Give the position of every malaria parasite and every leukocyte.
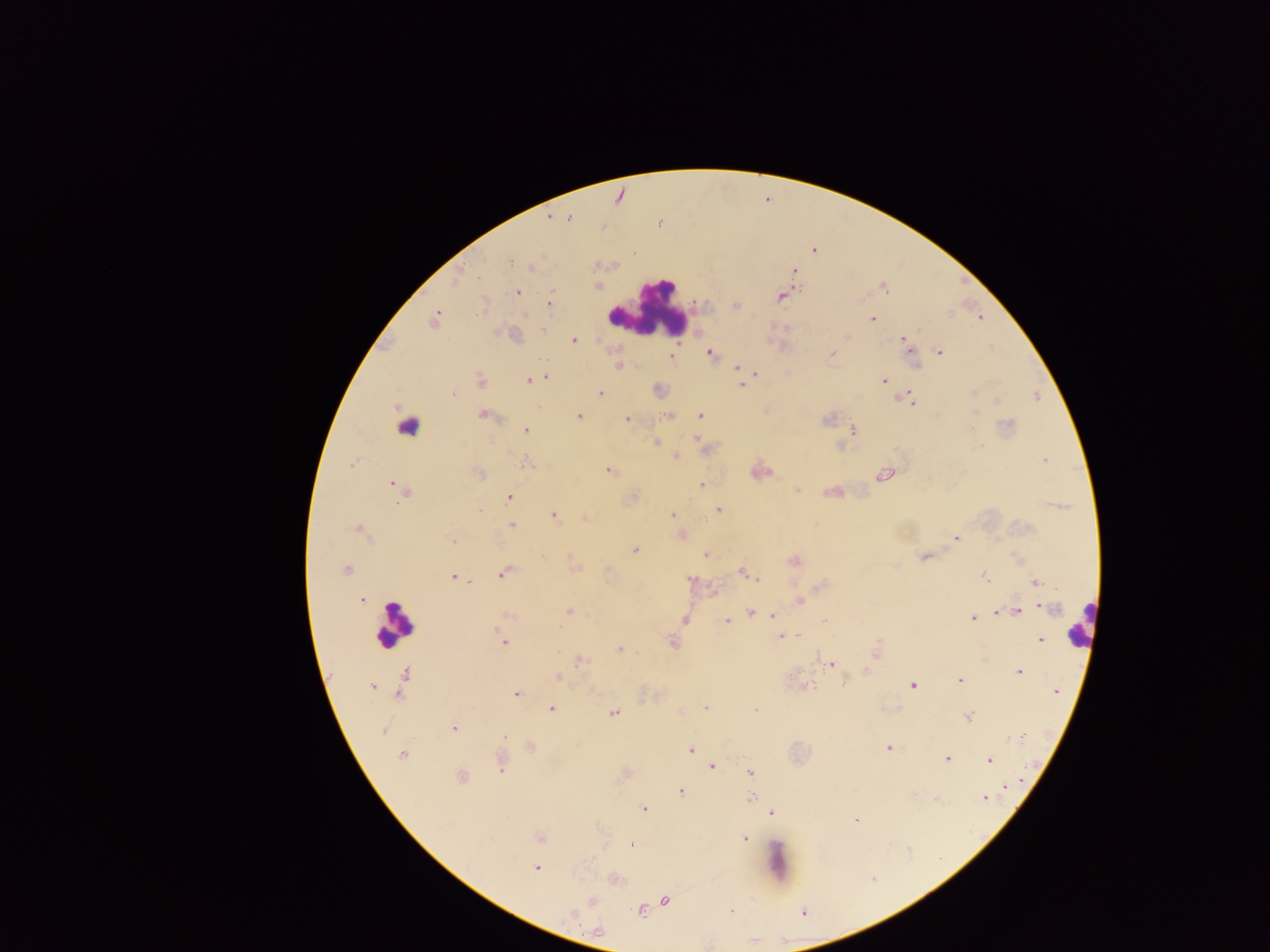
Approximate centers as [x, y] in pixels.
Malaria parasites: [551, 216], [566, 217], [659, 222], [812, 249], [509, 260], [529, 266], [794, 270], [458, 275], [884, 286], [518, 292], [782, 295], [549, 303], [735, 305], [435, 318], [872, 318], [979, 318], [543, 329], [846, 336], [903, 338], [573, 340], [910, 351], [939, 351], [710, 353], [832, 353], [671, 355], [618, 365], [736, 368], [751, 372], [755, 373], [545, 377], [883, 380], [528, 381], [480, 382], [742, 385], [658, 390], [972, 391], [452, 392], [599, 392], [909, 399], [914, 400], [997, 401], [483, 414], [669, 415], [701, 415], [579, 416], [627, 419], [853, 429], [526, 430], [696, 438], [655, 442], [839, 446], [674, 455], [1044, 459], [352, 463], [528, 463], [609, 470], [759, 471], [478, 473], [884, 474], [393, 484], [701, 486], [797, 489], [403, 492], [833, 492], [509, 497], [478, 510], [718, 510], [673, 514], [553, 515], [584, 518], [511, 525], [358, 529], [681, 534], [955, 538], [453, 540], [635, 549], [705, 554], [924, 557], [1019, 559], [794, 560], [574, 566], [345, 570], [741, 571], [504, 572], [984, 576], [454, 577], [757, 579], [691, 580], [1036, 582], [713, 592], [361, 599], [799, 600], [1040, 606], [568, 611], [1016, 611], [1003, 612], [997, 613], [749, 614], [506, 615], [773, 615], [972, 618], [684, 619], [726, 622], [798, 635], [780, 637], [1040, 639], [503, 641], [672, 643], [619, 649], [876, 651], [580, 660], [831, 664], [865, 671], [1019, 671], [558, 676], [405, 677], [960, 680], [843, 684], [912, 685], [373, 686], [803, 686], [401, 690], [592, 690], [1056, 691], [515, 693], [550, 708], [704, 708], [755, 710], [613, 712], [968, 716], [453, 728], [382, 730], [504, 736], [529, 747], [889, 748], [691, 749], [402, 754], [946, 758], [989, 760], [499, 763], [712, 765], [750, 772], [624, 773], [460, 777], [1004, 787], [681, 791], [751, 798], [984, 798], [643, 809], [771, 812], [854, 819], [539, 836], [743, 837], [630, 844], [535, 868], [613, 879], [664, 899], [592, 900], [639, 910], [572, 914].
Leukocytes: [649, 306], [407, 425], [393, 623], [1080, 625], [777, 861].

Summary:
  - Country: Ghana
  - Preparation: thick blood smear
  - Image size: 1270×952 pixels
  - Field of view: single
  - Capture: mobile-phone photograph through a microscope